Locate every blood parasite and identify its species.
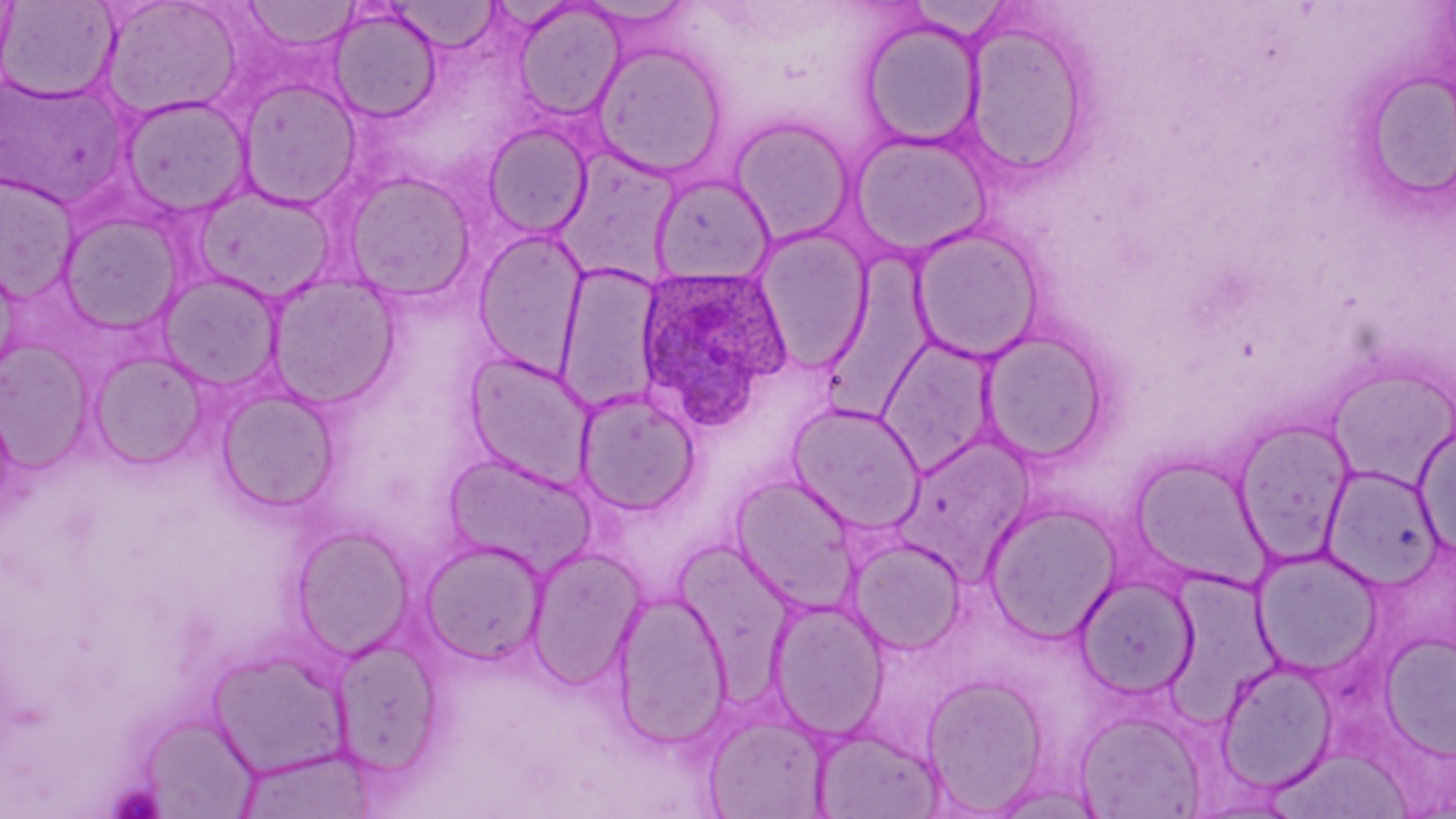
Approximate bounding boxes as [x1, y1, x2, y2] in pixels.
Plasmodium ovale-infected red blood cells: [634, 264, 793, 429].
No Plasmodium falciparum, Plasmodium malariae, Plasmodium vivax, Babesia divergens, or Trypanosoma brucei observed.

Summary:
  - Uninfected red blood cell locations: [0, 0, 120, 103], [99, 0, 245, 120], [242, 0, 360, 53], [388, 1, 501, 52], [511, 2, 625, 121], [328, 7, 442, 124], [962, 16, 1092, 178], [860, 17, 984, 148], [591, 40, 728, 180], [0, 74, 129, 207], [237, 77, 363, 210], [119, 95, 253, 217], [728, 115, 857, 247], [482, 123, 593, 238], [847, 129, 994, 260], [341, 170, 477, 301], [0, 173, 81, 301], [650, 173, 776, 285], [192, 184, 337, 302], [57, 210, 185, 334], [908, 225, 1046, 363], [749, 226, 874, 374], [472, 227, 590, 378], [820, 257, 936, 423], [555, 262, 664, 413], [155, 271, 285, 393], [265, 272, 401, 408], [977, 328, 1113, 465], [875, 333, 1001, 478], [0, 339, 95, 472], [87, 350, 209, 469], [461, 351, 598, 491], [1326, 365, 1456, 490], [215, 386, 340, 512], [574, 388, 701, 515], [785, 401, 927, 535], [1232, 417, 1357, 565], [1414, 425, 1456, 561], [894, 435, 1036, 576], [443, 453, 597, 578], [1126, 453, 1274, 593], [1321, 464, 1444, 590], [729, 473, 863, 613], [983, 501, 1123, 643], [290, 524, 415, 659], [845, 535, 967, 655], [419, 539, 549, 665], [524, 545, 647, 689], [1254, 548, 1385, 676], [1075, 574, 1199, 700], [609, 587, 733, 750], [767, 596, 890, 740], [1380, 632, 1456, 760], [330, 636, 444, 775], [205, 646, 353, 779], [1215, 658, 1339, 793], [920, 673, 1050, 812], [1073, 709, 1208, 818], [702, 713, 830, 818], [139, 714, 260, 818], [810, 725, 946, 819], [230, 746, 378, 818], [1274, 748, 1413, 817]
  - Slide-level diagnosis: Plasmodium ovale
  - Magnification: 1000x
  - Modality: light microscopy
  - Stain: May-Grünwald-Giemsa
  - Preparation: thin blood film
  - Field of view: one of a larger specimen
  - Image size: 1456×819 pixels